Assess the morphology of the erythrocytes.
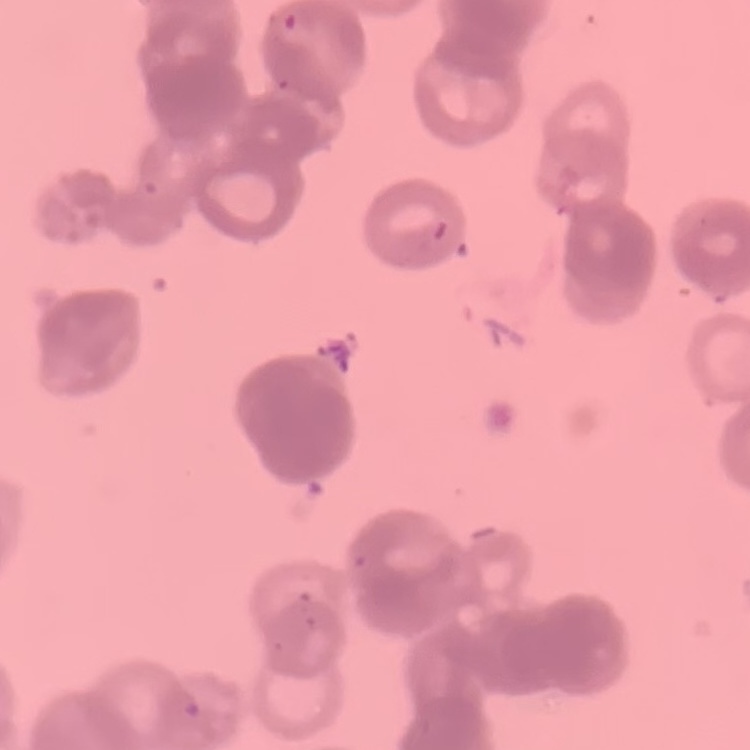

They show rouleaux formation.

Stained with either Field's or Giemsa. Thin peripheral smear. One tile cut from a larger photomicrograph.